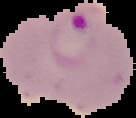

Summary:
  - Image type: segmented cell region on a black background
  - Preparation: thin blood film
  - Result: malaria parasites detected
  - Image size: 136×118 pixels